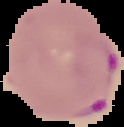
Summary:
  - Image type: segmented cell region on a black background
  - Image size: 124×127 pixels
  - Malaria status: parasitized
  - Preparation: thin blood film